Give the extent of all Plasmodium falciparum-infected red blood cells.
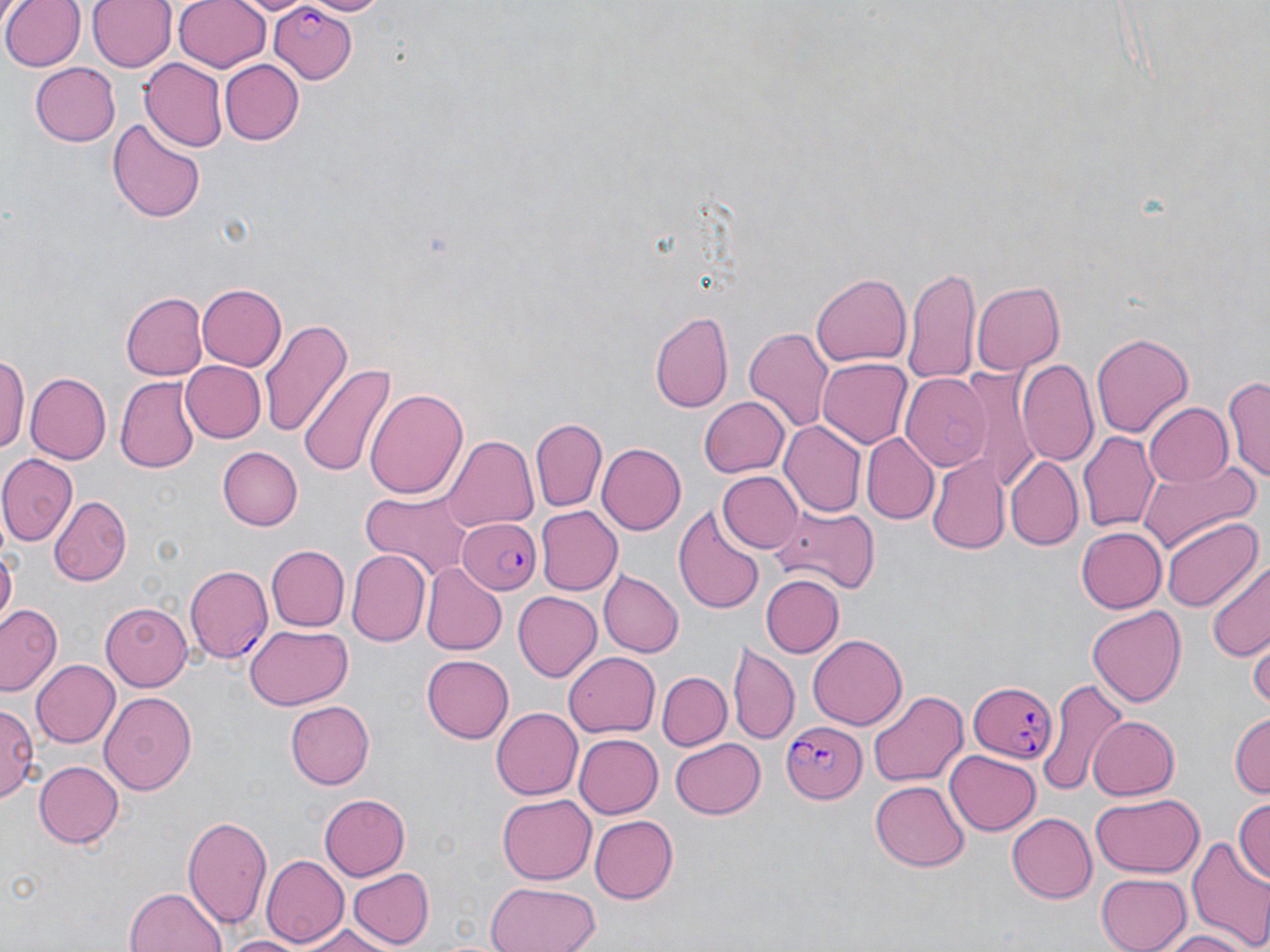
Approximate bounding boxes as (x1,y1)-(x2,y2) corner pairs in pixels.
Plasmodium falciparum-infected red blood cells: (265,4)-(357,83), (458,517)-(545,595), (185,564)-(273,664), (968,679)-(1058,762), (780,720)-(865,804).

Summary:
  - Uninfected red blood cell locations: (2,0)-(81,71), (89,0)-(177,73), (172,0)-(272,72), (238,0)-(311,17), (219,59)-(304,145), (139,60)-(227,152), (28,62)-(119,145), (107,117)-(205,224), (905,264)-(981,389), (811,271)-(912,368), (972,280)-(1064,374), (197,283)-(287,372), (121,291)-(207,379), (649,309)-(735,415), (259,317)-(350,438), (742,325)-(834,435), (1090,330)-(1194,439), (0,350)-(28,462), (961,357)-(1045,494), (817,358)-(912,449), (179,359)-(265,442), (1015,359)-(1099,467), (298,363)-(396,475), (27,373)-(111,463), (900,374)-(991,471), (1223,374)-(1270,484), (116,377)-(201,473), (365,387)-(468,500), (699,394)-(789,477), (1141,402)-(1231,488), (530,417)-(607,513), (778,421)-(865,518), (1079,431)-(1159,535), (863,434)-(938,524), (442,435)-(537,534), (596,442)-(687,535), (216,446)-(303,530), (927,451)-(1008,553), (0,453)-(79,547), (1004,456)-(1082,552), (1139,462)-(1260,553), (717,471)-(803,554), (358,490)-(478,581), (49,496)-(130,586), (673,504)-(767,615), (767,505)-(882,593), (534,506)-(623,597), (1161,517)-(1259,613), (1074,527)-(1165,613), (0,541)-(18,630), (266,545)-(349,632), (346,550)-(429,648), (1207,562)-(1269,662), (421,563)-(506,656), (591,564)-(694,730), (598,570)-(684,658), (760,574)-(843,656), (512,592)-(603,680), (100,601)-(195,689), (0,604)-(62,693), (1085,605)-(1186,709), (245,625)-(353,711), (808,636)-(907,728), (1249,641)-(1269,714), (729,642)-(798,744), (563,651)-(661,738), (422,652)-(514,742), (30,658)-(120,749), (657,671)-(732,750), (1036,683)-(1124,793), (868,690)-(968,787), (99,691)-(197,796), (284,701)-(372,789), (0,704)-(41,802), (491,707)-(585,799), (1230,712)-(1269,802), (1087,714)-(1179,801), (574,734)-(662,817), (670,738)-(767,819), (945,749)-(1041,835), (33,761)-(123,847), (868,778)-(971,871), (498,792)-(595,882), (1090,793)-(1205,879), (319,794)-(409,881), (1232,798)-(1270,883), (183,812)-(274,931), (1007,813)-(1096,902), (590,814)-(678,904), (1186,836)-(1270,947), (263,853)-(348,948), (347,867)-(434,949), (1094,872)-(1193,952), (485,880)-(600,952), (124,886)-(228,952), (293,923)-(400,952), (1153,929)-(1257,952), (218,933)-(314,952)
  - Slide-level diagnosis: Plasmodium falciparum
  - Modality: optical microscopy
  - Image size: 1270×952 pixels
  - Stain: May-Grünwald-Giemsa
  - Magnification: 1000x
  - Field of view: one of a larger specimen
  - Preparation: thin blood film